Classify this cell by malaria status.
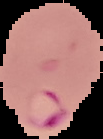

Parasitized.

Summary:
  - Preparation: thin blood film
  - Image type: segmented cell region with the area outside set to black
  - Image size: 103×139 pixels